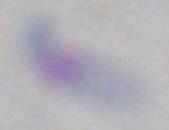
Summary:
  - Magnification: 1000x
  - Modality: photomicrograph
  - Identification: Toxoplasma gondii